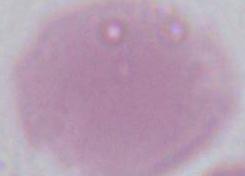 Micrograph. A red blood cell is seen. Captured at 1000x magnification.